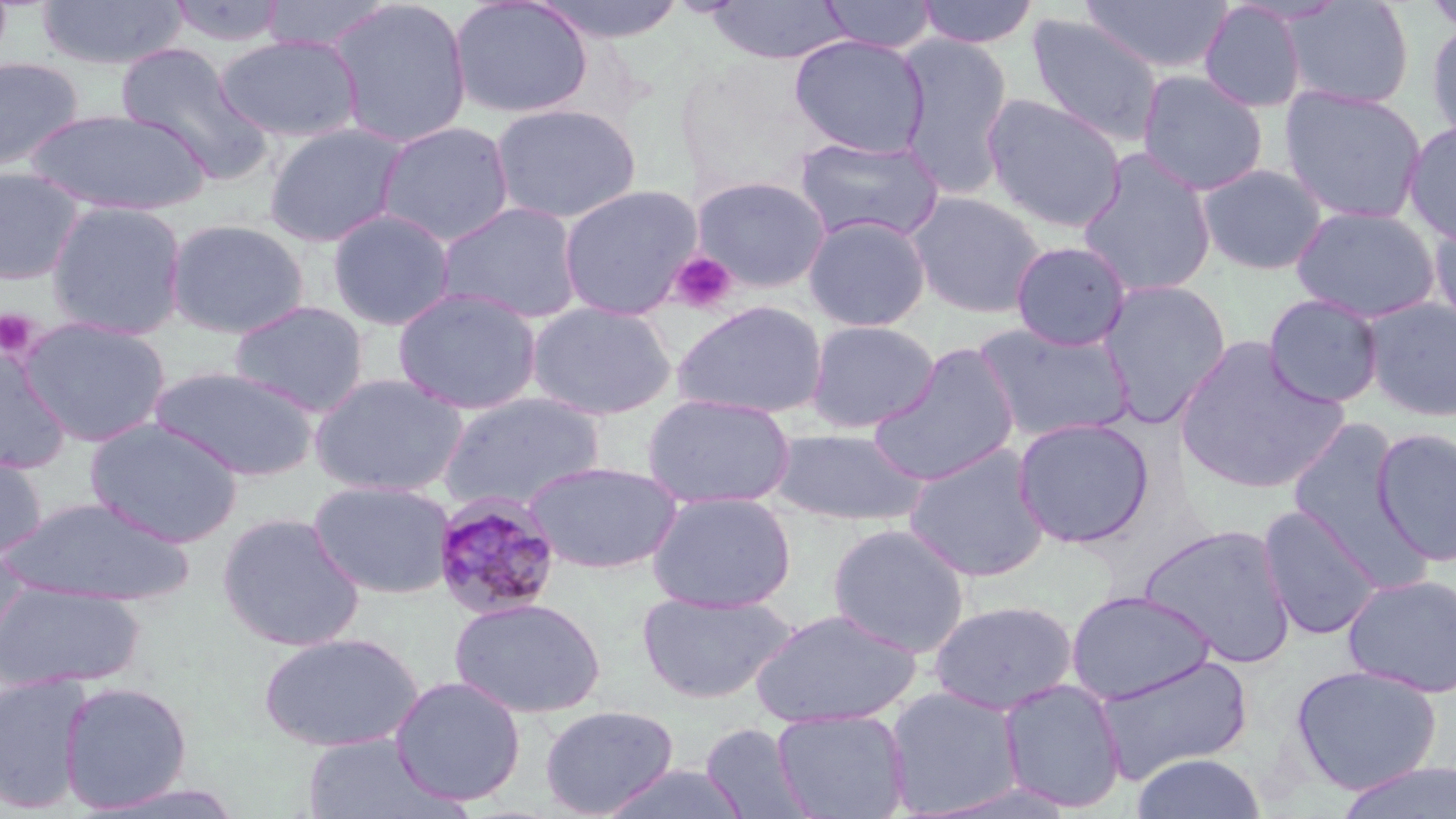 Approximate bounding boxes as (x1, y1, x2, y2) in pixels. Platelet locations: (668, 250, 737, 314), (0, 309, 39, 358). Plasmodium malariae-infected red blood cell locations: (431, 491, 564, 621). Uninfected red blood cell locations: (35, 0, 188, 71), (261, 0, 395, 53), (327, 0, 473, 148), (450, 0, 592, 119), (529, 0, 689, 43), (818, 0, 938, 53), (915, 0, 1039, 48), (1080, 0, 1233, 76), (1422, 0, 1456, 37), (166, 1, 289, 47), (707, 1, 850, 64), (1199, 1, 1308, 113), (1281, 1, 1416, 110), (1025, 12, 1163, 147), (1425, 20, 1456, 146), (215, 34, 363, 143), (789, 35, 930, 158), (896, 36, 1014, 198), (115, 41, 271, 182), (0, 55, 85, 172), (675, 56, 833, 196), (1136, 69, 1269, 196), (1279, 85, 1428, 224), (982, 93, 1127, 233), (491, 103, 642, 224), (26, 108, 209, 217), (1402, 120, 1456, 246), (375, 121, 515, 247), (263, 122, 409, 247), (792, 135, 945, 245), (1076, 148, 1218, 298), (1196, 163, 1328, 276), (0, 166, 88, 285), (692, 174, 831, 292), (559, 184, 703, 321), (906, 191, 1047, 318), (46, 200, 188, 340), (435, 200, 584, 324), (1290, 204, 1441, 323), (327, 208, 456, 330), (803, 214, 932, 332), (1428, 215, 1456, 338), (165, 218, 310, 339), (1010, 241, 1132, 350), (1097, 279, 1231, 427), (392, 287, 542, 415), (1262, 293, 1385, 409), (1361, 297, 1456, 421), (228, 300, 369, 417), (672, 300, 829, 418), (526, 301, 677, 421), (17, 316, 172, 447), (805, 320, 940, 433), (974, 322, 1135, 443), (1173, 337, 1351, 494), (868, 343, 1021, 486), (0, 351, 71, 471), (148, 365, 319, 481), (308, 372, 468, 497), (438, 392, 606, 511), (641, 393, 796, 510), (1012, 416, 1155, 549), (1283, 417, 1420, 571), (86, 419, 243, 547), (768, 426, 928, 526), (1372, 427, 1456, 567), (904, 443, 1051, 583), (0, 448, 47, 561), (523, 459, 682, 574), (309, 478, 456, 599), (646, 490, 796, 613), (3, 495, 194, 606), (1257, 504, 1384, 641), (217, 512, 365, 652), (827, 522, 971, 657), (1138, 522, 1297, 668), (0, 543, 31, 659), (1342, 572, 1456, 698), (0, 581, 145, 691), (1066, 589, 1216, 705), (636, 590, 797, 704), (450, 597, 606, 717), (928, 599, 1079, 715), (749, 607, 921, 728), (258, 631, 424, 753), (1091, 652, 1254, 783), (1290, 663, 1443, 795), (0, 672, 93, 815), (389, 675, 527, 806), (997, 678, 1127, 813), (59, 680, 193, 813), (884, 685, 1026, 817), (539, 704, 679, 818), (771, 709, 911, 819), (701, 721, 815, 818), (300, 733, 460, 818), (1129, 752, 1267, 819), (1333, 761, 1456, 819), (596, 763, 751, 819), (920, 779, 1080, 818). Slide-level diagnosis: Plasmodium malariae. Optical microscopy. Thin blood film. May-Grünwald-Giemsa stain. Single field of view. Image is 1456×819 pixels. 1000x magnification.